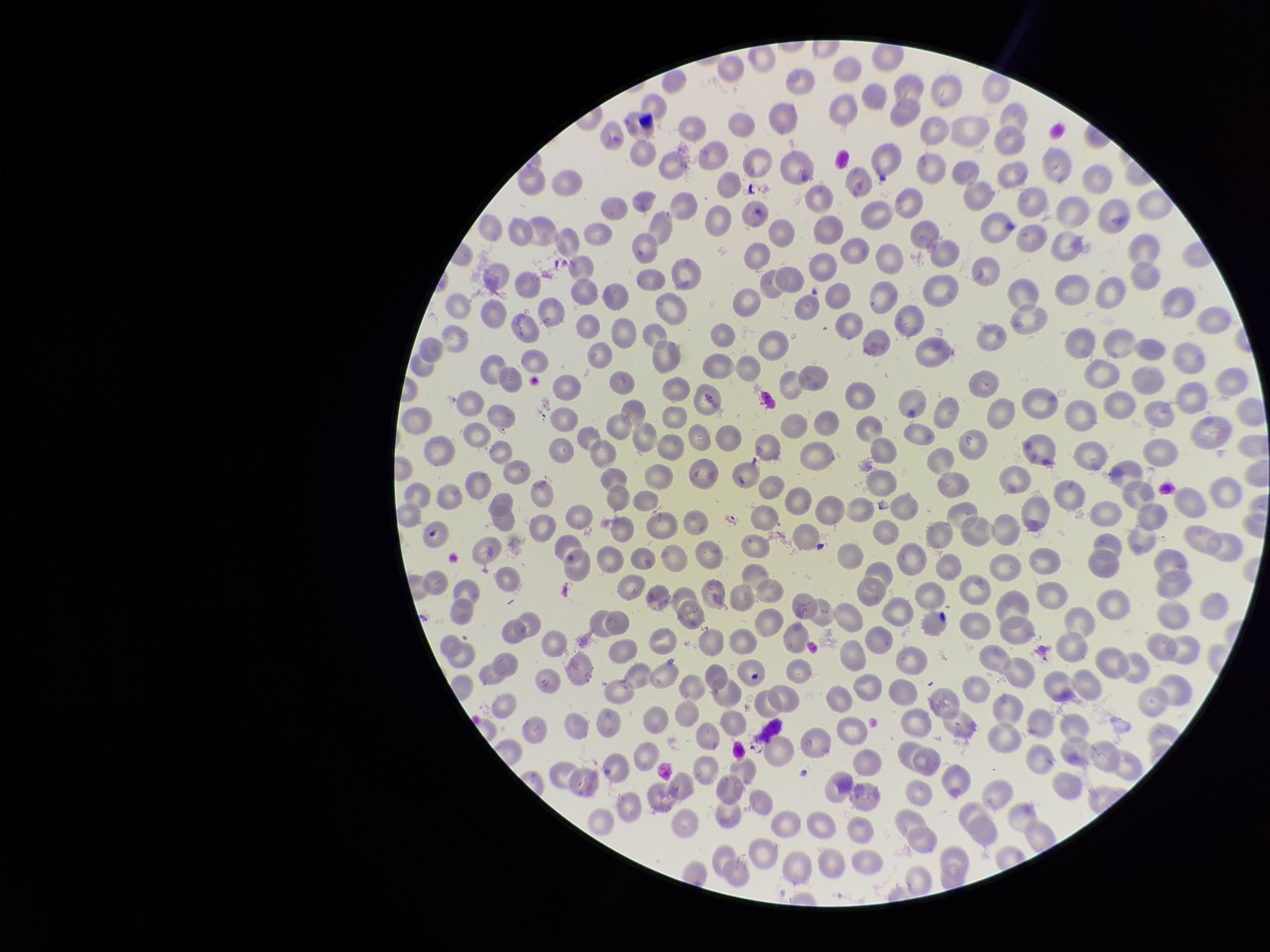
Red blood cell count: 325. Patient malaria status: negative. Smartphone photograph taken through the eyepiece of a microscope. Parasitized red blood cell count: 0. Image is 1270×952 pixels. Single field of view. Preparation: thin smear. Giemsa stain. Parasitized red blood cells: none detected.